Comment on the morphology of the erythrocytes.
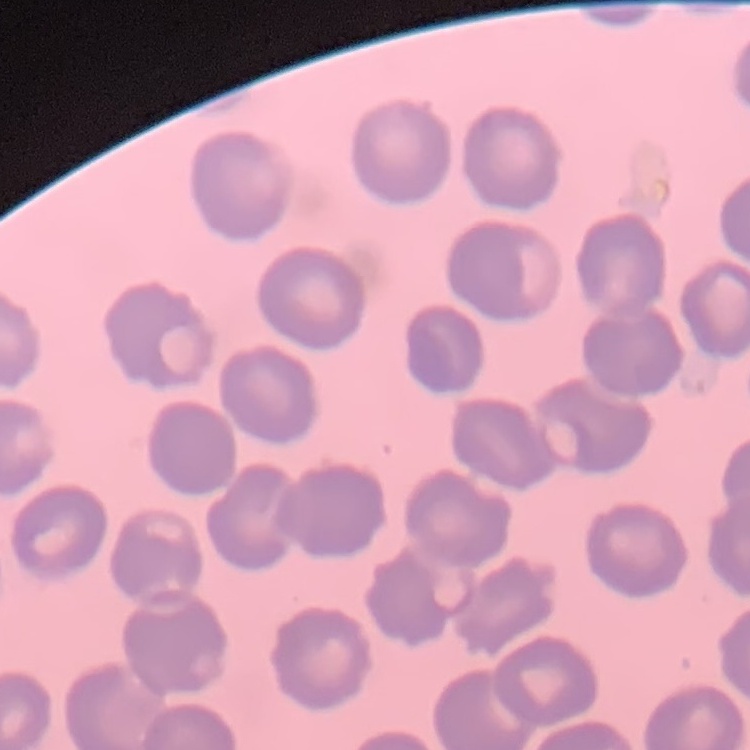
They show no rouleaux formation.

stain = Field's or Giemsa
preparation = thin blood smear
image type = square crop of a larger photomicrograph